State which parasite is depicted.
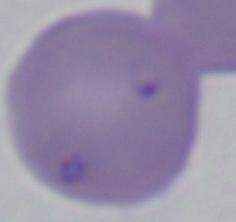

This is Babesia.

{
  "modality": "photomicrograph",
  "magnification": "1000x"
}